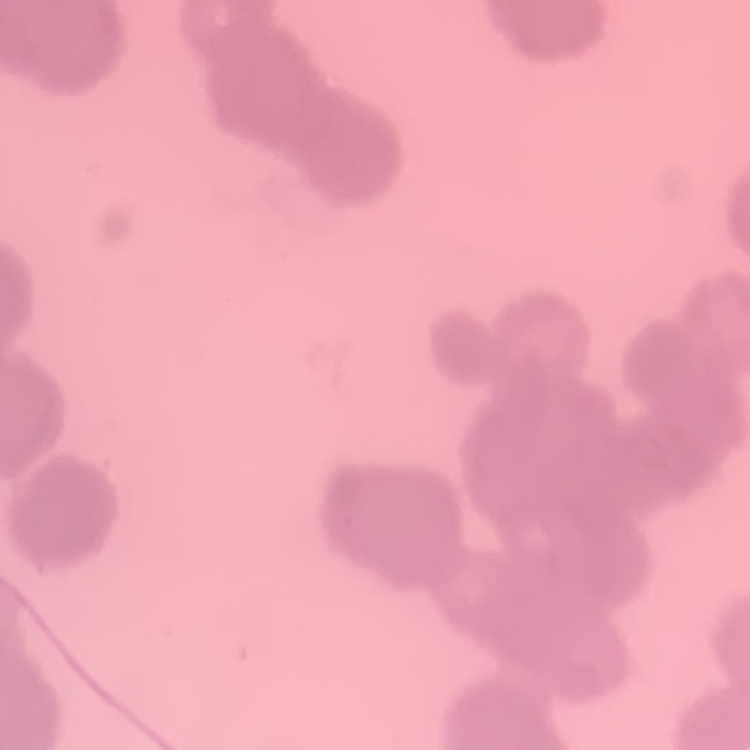
Summary:
  - Erythrocyte morphology: rouleaux formation
  - Image type: one tile cut from a larger photomicrograph
  - Preparation: thin peripheral smear
  - Stain: Field's or Giemsa